Outline each Plasmodium falciparum-infected red blood cell.
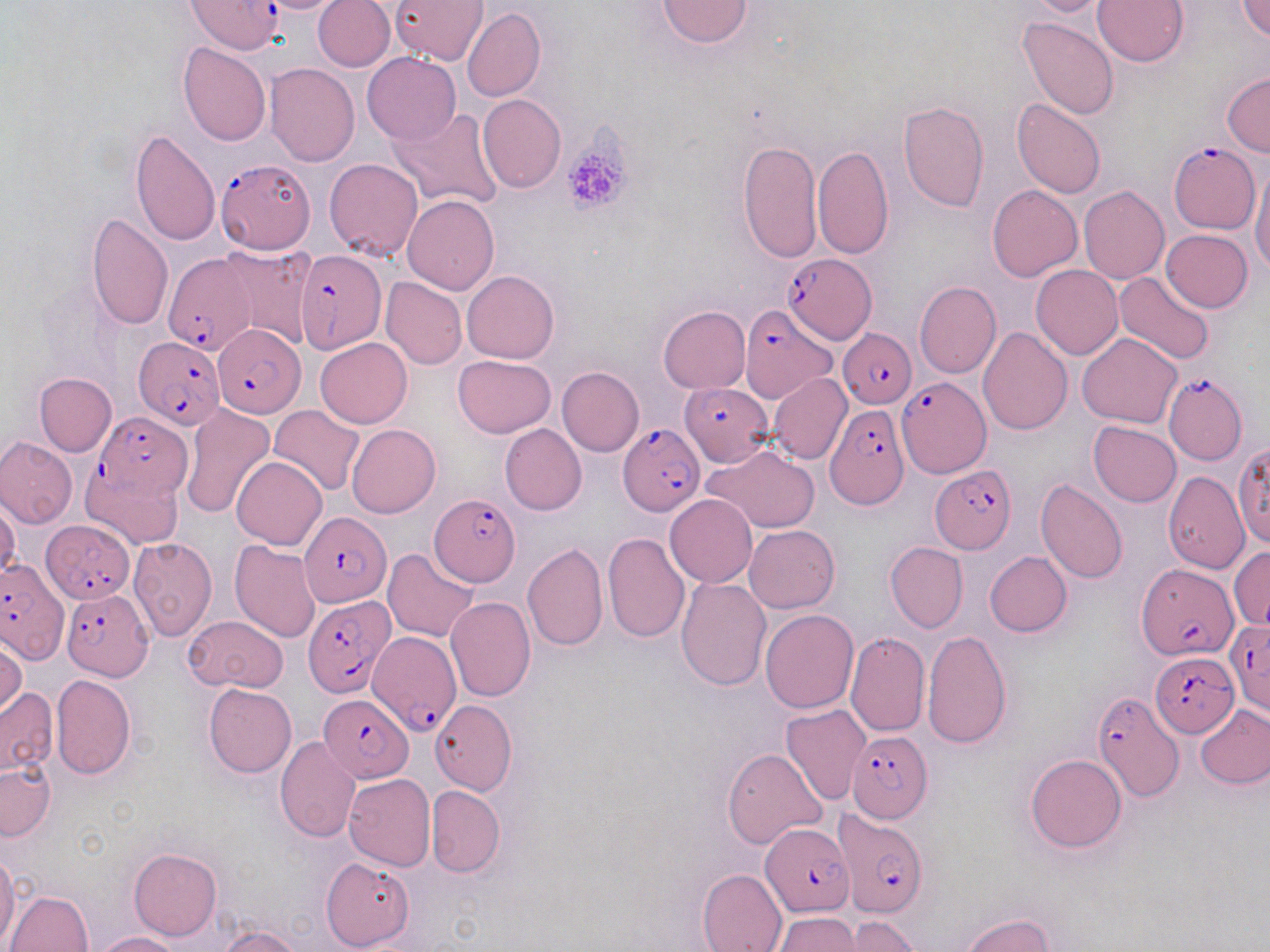
Approximate bounding boxes as (x1, y1, x2, y2) in pixels.
Plasmodium falciparum-infected red blood cells: (189, 1, 282, 55), (1167, 142, 1262, 235), (215, 159, 316, 254), (294, 249, 386, 354), (165, 250, 260, 353), (782, 251, 878, 344), (740, 306, 834, 403), (213, 324, 305, 417), (838, 330, 916, 407), (132, 335, 226, 430), (1162, 372, 1248, 465), (898, 378, 991, 477), (680, 384, 773, 466), (826, 403, 908, 509), (95, 414, 193, 498), (619, 423, 704, 515), (931, 466, 1016, 555), (430, 493, 523, 587), (298, 512, 390, 607), (41, 520, 135, 603), (0, 560, 65, 661), (1137, 563, 1236, 660), (61, 588, 154, 680), (303, 594, 396, 697), (1226, 622, 1270, 718), (366, 634, 463, 731), (1154, 651, 1240, 733), (1092, 692, 1185, 803), (318, 693, 413, 782), (844, 731, 933, 823), (835, 811, 927, 917), (760, 823, 856, 916).

Summary:
  - Platelet locations: (561, 142, 630, 214)
  - Uninfected red blood cell locations: (252, 0, 348, 13), (314, 0, 395, 72), (391, 0, 487, 65), (658, 0, 752, 48), (1025, 0, 1112, 18), (1094, 0, 1187, 67), (1236, 0, 1270, 40), (463, 6, 545, 101), (1020, 17, 1119, 120), (177, 42, 272, 148), (362, 52, 460, 144), (265, 64, 360, 166), (1222, 73, 1270, 157), (478, 94, 566, 193), (1012, 99, 1105, 199), (898, 100, 989, 211), (385, 106, 504, 210), (130, 129, 220, 246), (738, 140, 822, 262), (812, 144, 893, 259), (325, 158, 424, 261), (1251, 165, 1270, 275), (988, 185, 1082, 281), (1080, 186, 1170, 284), (403, 196, 499, 295), (87, 213, 174, 331), (1161, 229, 1253, 312), (220, 244, 316, 351), (1030, 266, 1122, 360), (463, 269, 559, 362), (1114, 270, 1215, 364), (381, 278, 466, 369), (914, 281, 1001, 379), (657, 306, 750, 393), (977, 327, 1072, 435), (1077, 333, 1182, 428), (315, 337, 412, 427), (453, 355, 556, 437), (557, 366, 644, 455), (33, 373, 116, 457), (769, 373, 852, 464), (180, 403, 276, 519), (269, 405, 365, 495), (1089, 421, 1181, 507), (500, 423, 587, 515), (346, 424, 440, 518), (0, 437, 77, 527), (701, 441, 821, 534), (1228, 445, 1270, 557), (231, 457, 327, 549), (82, 466, 183, 549), (1161, 471, 1250, 574), (1036, 477, 1129, 583), (665, 494, 757, 588), (0, 498, 20, 581), (744, 524, 839, 612), (603, 533, 689, 645), (128, 537, 218, 641), (230, 540, 322, 643), (885, 541, 967, 633), (522, 543, 609, 651), (1229, 545, 1270, 633), (383, 548, 480, 642), (984, 551, 1072, 637), (676, 575, 772, 690), (445, 596, 536, 702), (760, 610, 859, 713), (185, 616, 288, 693), (923, 630, 1012, 749), (844, 631, 929, 736), (0, 635, 25, 719), (51, 674, 136, 781), (204, 683, 296, 777), (0, 688, 57, 777), (429, 700, 517, 796), (781, 704, 872, 806), (1195, 704, 1270, 789), (274, 735, 361, 842), (722, 747, 827, 848), (1025, 754, 1127, 853), (0, 760, 56, 841), (343, 773, 436, 871), (427, 784, 505, 878), (129, 847, 222, 939), (0, 850, 20, 950), (322, 857, 412, 951), (696, 867, 788, 952), (6, 890, 92, 951), (772, 913, 862, 950), (964, 913, 1058, 952), (843, 916, 922, 951), (217, 926, 302, 952), (96, 932, 183, 952)
  - Slide-level diagnosis: Plasmodium falciparum
  - Field of view: one of a larger specimen
  - Preparation: thin blood smear
  - Magnification: 1000x
  - Stain: May-Grünwald-Giemsa
  - Image size: 1270×952 pixels
  - Modality: optical microscopy